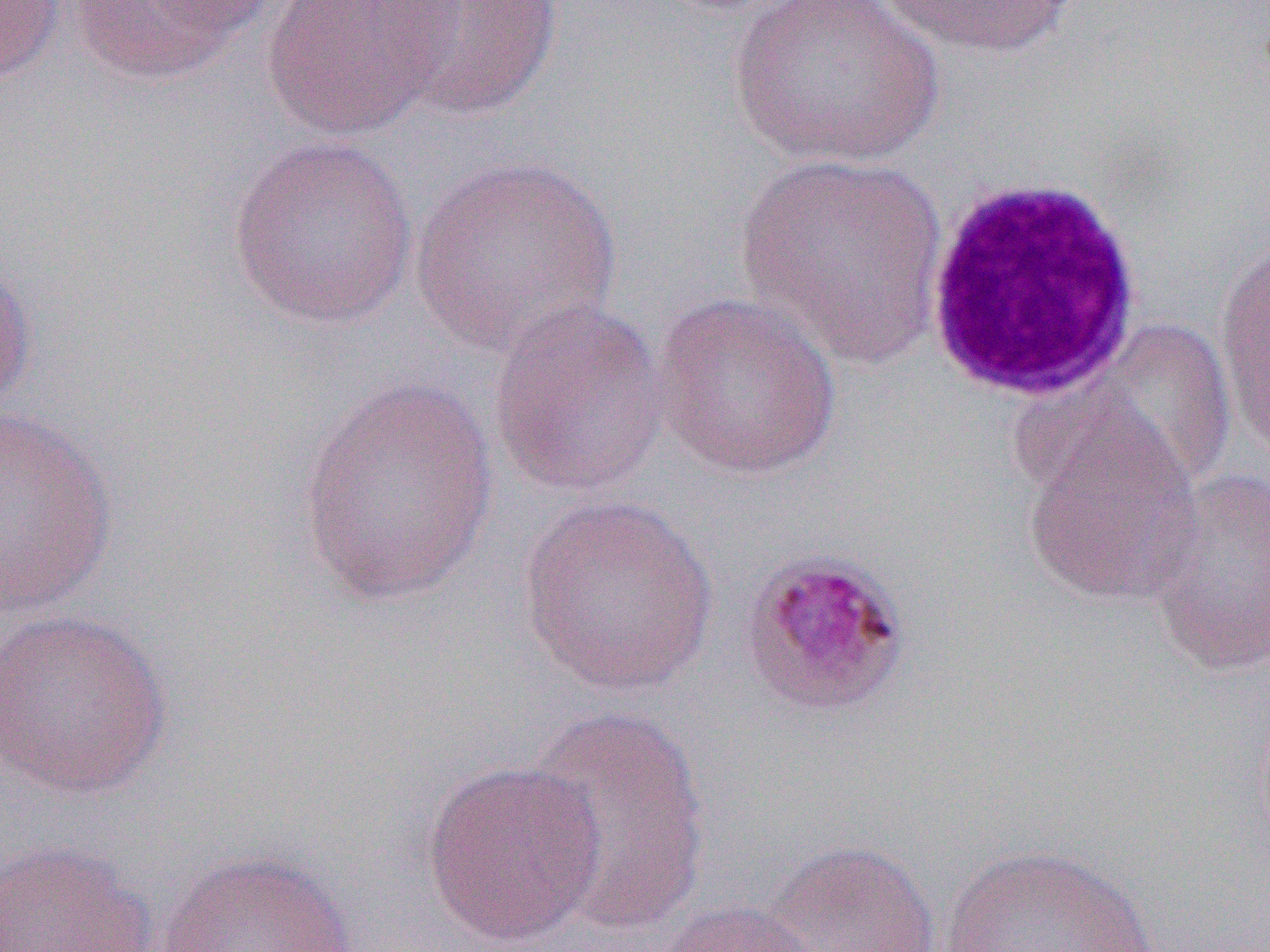
{
  "slide_level_diagnosis": "Plasmodium malariae",
  "uninfected_red_blood_cell_locations": "approximate bounding boxes as (x1, y1, x2, y2) in pixels: (63, 0, 272, 85), (261, 0, 456, 142), (726, 0, 946, 170), (0, 1, 66, 84), (387, 1, 564, 122), (878, 1, 1080, 60), (227, 135, 419, 330), (733, 151, 952, 370), (406, 154, 624, 356), (1214, 230, 1270, 466), (0, 255, 38, 423), (650, 291, 844, 482), (486, 297, 671, 498), (1084, 318, 1240, 494), (298, 375, 500, 607), (1018, 400, 1204, 608), (0, 406, 120, 621), (1144, 468, 1270, 679), (517, 495, 719, 698), (0, 608, 173, 800), (521, 708, 713, 933), (420, 757, 607, 948), (0, 837, 158, 952), (766, 839, 943, 951), (941, 844, 1165, 952), (157, 847, 357, 952), (651, 898, 830, 952)",
  "preparation": "thin blood smear",
  "magnification": "1000x",
  "field_of_view": "single",
  "modality": "optical microscopy",
  "image_size": "1270×952 pixels",
  "white_blood_cell_locations": "approximate bounding boxes as (x1, y1, x2, y2) in pixels: (921, 173, 1146, 403)"
}